Classify this cell by malaria status.
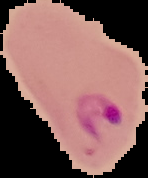

It is parasitized.

Image is 148×178 pixels. From a thin blood smear. The area outside the segmented cell region is set to black.